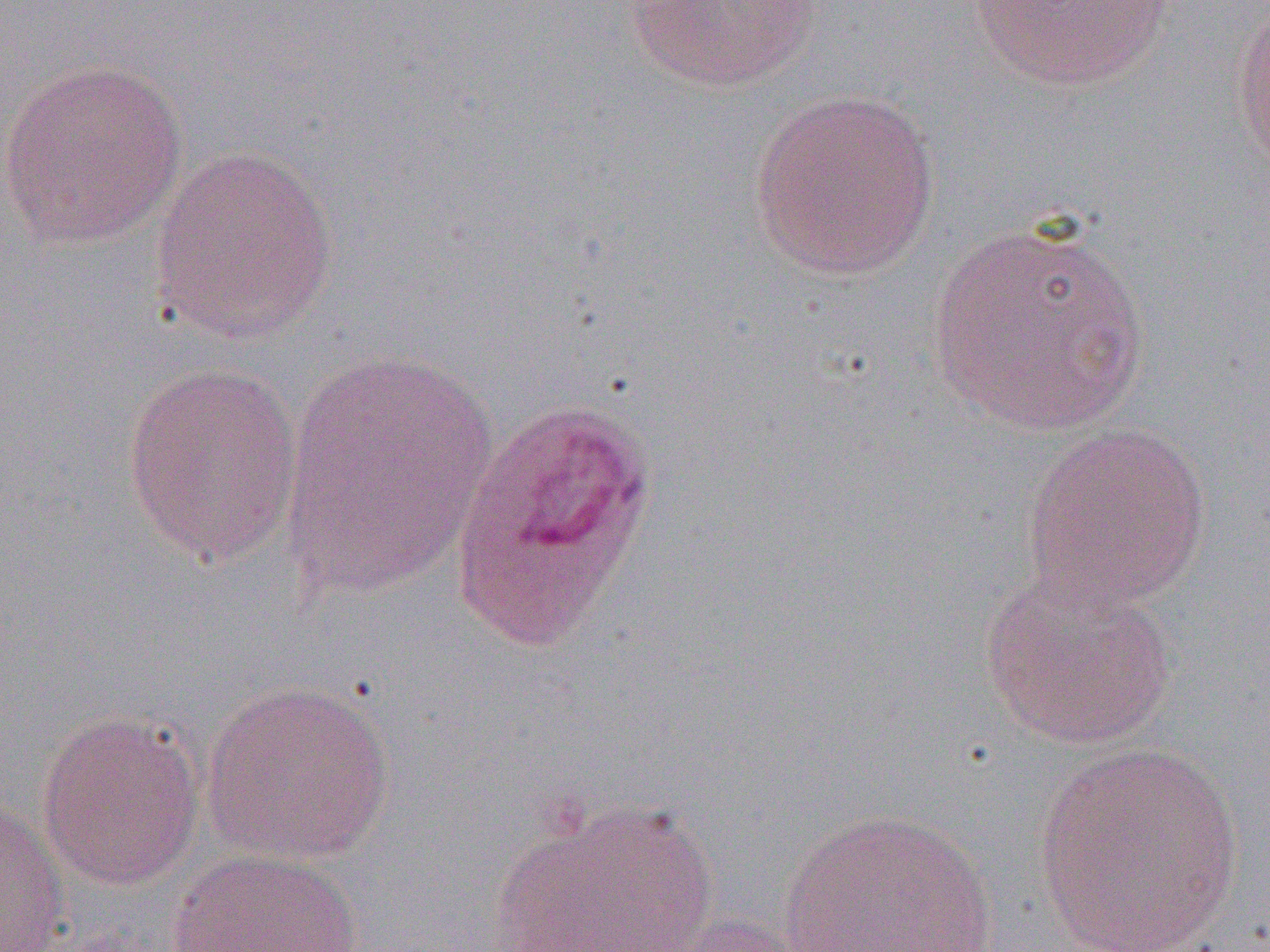
Summary:
  - Coordinate format: approximate bounding boxes as [x1, y1, x2, y2] in pixels
  - Plasmodium ovale-infected red blood cell locations: [449, 397, 661, 651]
  - Uninfected red blood cell locations: [622, 0, 824, 93], [968, 0, 1175, 92], [1229, 4, 1270, 176], [0, 56, 189, 251], [747, 88, 942, 281], [149, 145, 340, 345], [925, 217, 1151, 437], [280, 349, 498, 600], [120, 361, 306, 569], [1021, 421, 1213, 613], [979, 569, 1179, 752], [201, 678, 396, 865], [35, 709, 207, 892], [1032, 744, 1244, 950], [0, 794, 70, 952], [487, 798, 721, 952], [780, 808, 999, 951], [166, 848, 364, 952], [666, 915, 814, 952]
  - Slide-level diagnosis: Plasmodium ovale
  - Magnification: 1000x
  - Field of view: single
  - Preparation: thin blood film
  - Modality: light microscopy
  - Image size: 1270×952 pixels